Assess this cell for malaria.
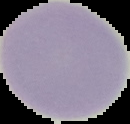

It is uninfected.

Summary:
  - Preparation: thin blood smear
  - Image type: segmented cell region on a black background
  - Image size: 130×124 pixels